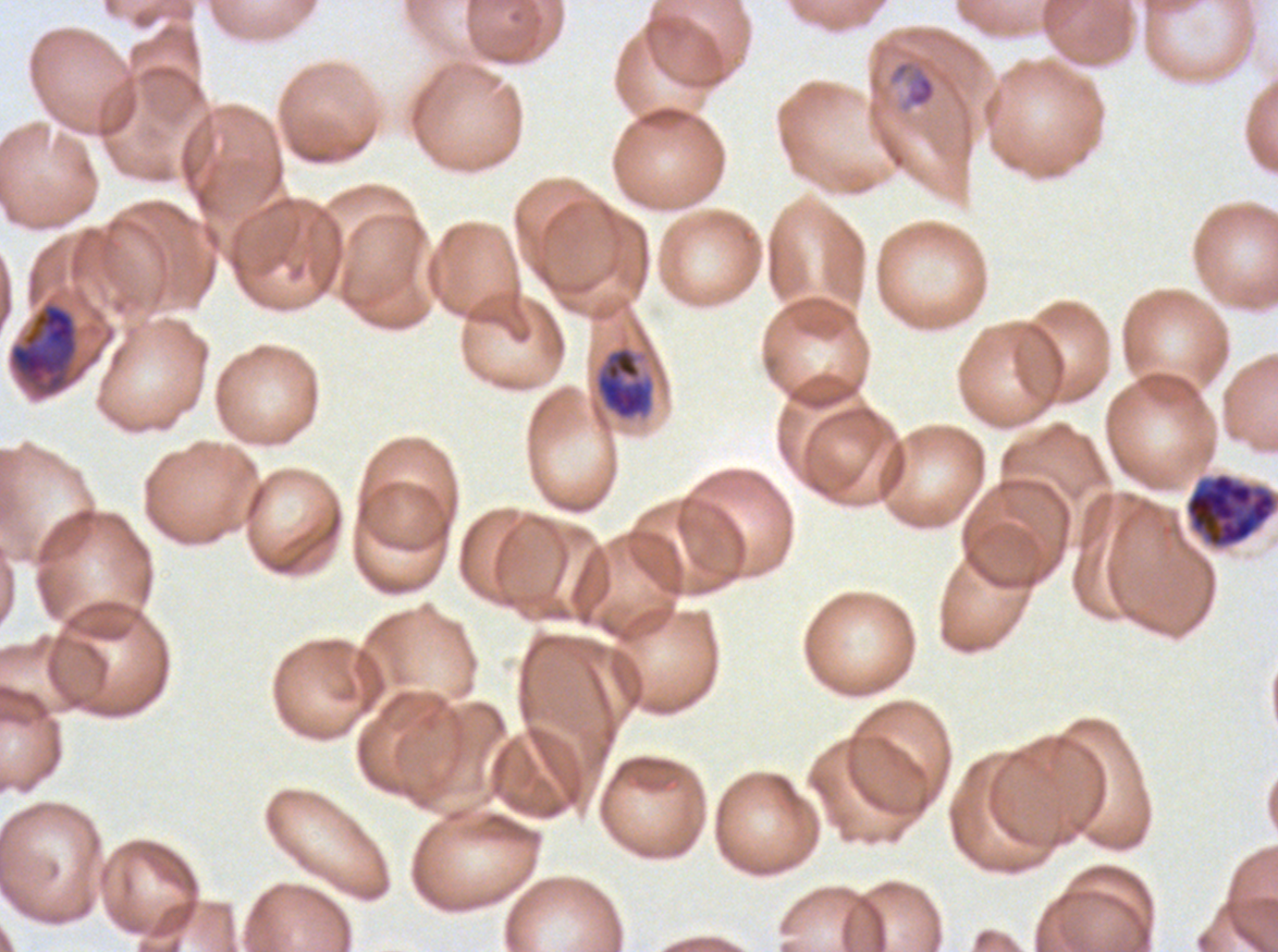

Approximate bounding rectangles given as corner coordinates in pixels from the top-left. Late-ring/early-trophozoite locations: (x1=889, y1=60, x2=937, y2=108). Late schizont locations: (x1=1185, y1=472, x2=1277, y2=549). Mid trophozoite locations: (x1=594, y1=345, x2=656, y2=421). Early schizont locations: (x1=8, y1=301, x2=79, y2=397). One sub-image of a larger composite. Life-cycle stages observed: late-ring/early-trophozoite, mid trophozoite, early schizont, late schizont. Thin blood smear. Giemsa-stained preparation. Plasmodium falciparum cultured ex vivo for 24 to 48 hours, from a patient in The Gambia. Image is 1278×952 pixels.